Point out each Plasmodium parasite and each leukocyte.
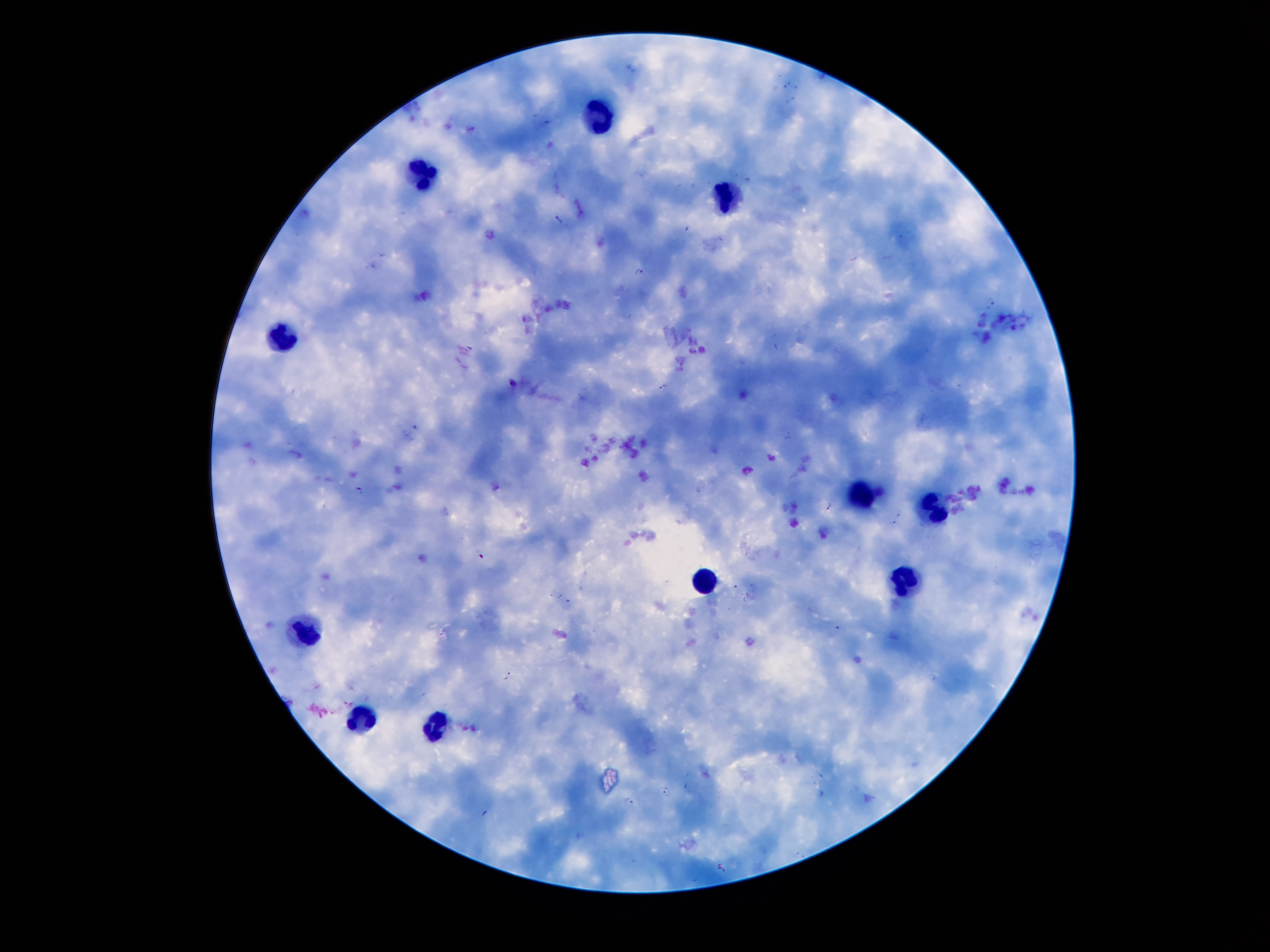
Approximate centers as (x, y) in pixels.
Plasmodium parasites: (560, 215), (639, 271), (514, 383), (663, 386), (360, 490), (830, 506), (900, 514), (892, 524), (509, 676), (665, 791), (626, 800).
Leukocytes: (599, 119), (422, 176), (726, 198), (276, 337), (859, 494), (933, 512), (901, 577), (705, 582), (300, 629), (357, 716), (435, 728).

stain: Giemsa
patient_malaria_status: infected with Plasmodium falciparum
magnification: 100x
preparation: thick blood smear
image_size: 1270×952 pixels
field_of_view: single
capture: smartphone camera through the microscope eyepiece